Report the malaria status of this cell.
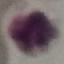

Uninfected.

stain: Giemsa
capture: smartphone through the microscope eyepiece
image_type: cell patch, automatically extracted from a larger field of view and resized to 64 × 64 pixels
preparation: thin blood smear